Give the extent of all Plasmodium vivax-infected red blood cells.
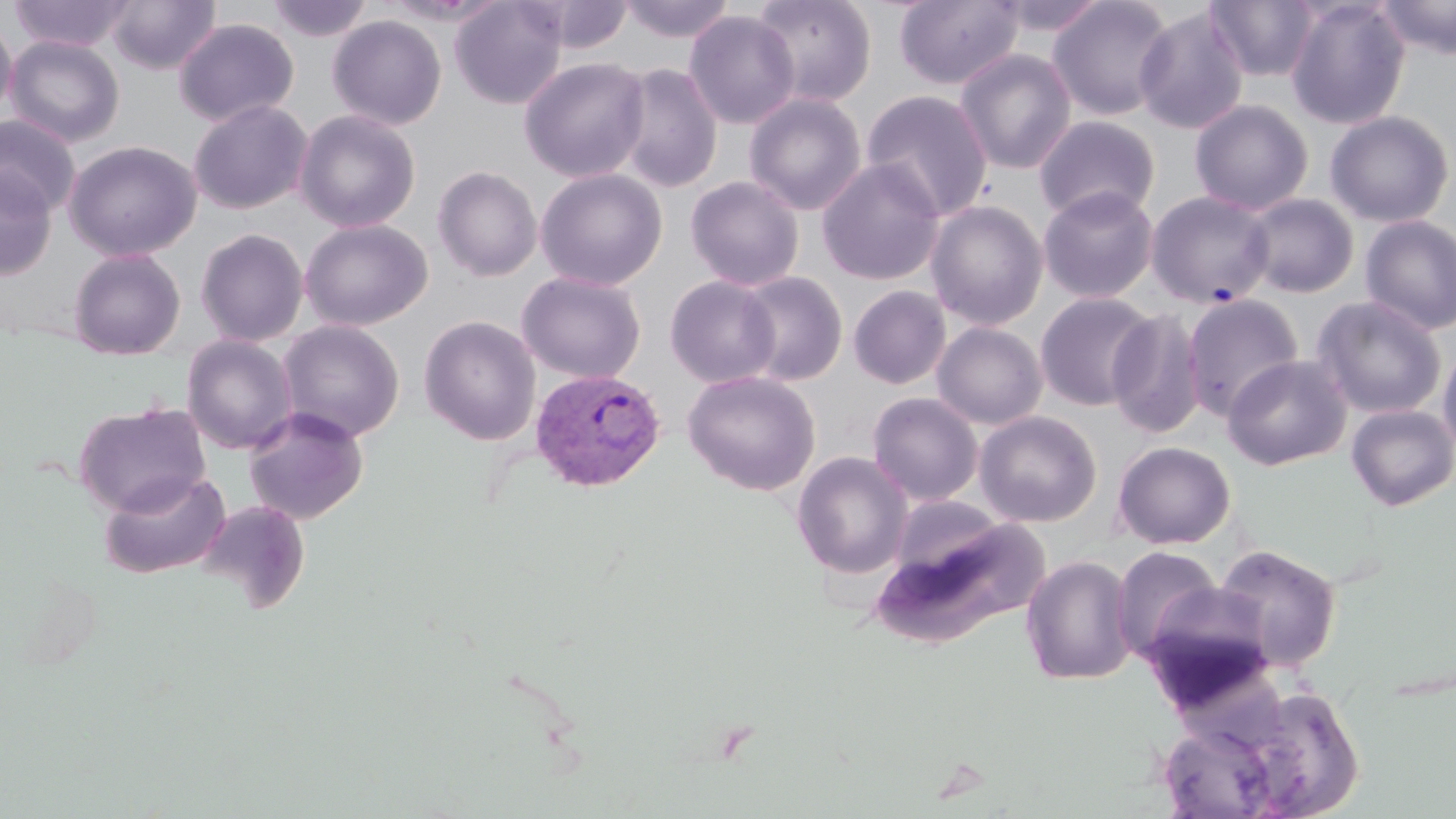

Approximate bounding boxes as named x1/y1/x2/y2 corners in pixels.
Plasmodium vivax-infected red blood cells: (x1=529, y1=368, x2=666, y2=493).

slide-level diagnosis = Plasmodium vivax
modality = light microscopy
preparation = thin blood smear
uninfected red blood cell locations = approximate bounding boxes as named x1/y1/x2/y2 corners in pixels: (x1=8, y1=0, x2=134, y2=52), (x1=106, y1=0, x2=221, y2=74), (x1=267, y1=0, x2=372, y2=43), (x1=450, y1=0, x2=568, y2=109), (x1=528, y1=0, x2=635, y2=53), (x1=621, y1=0, x2=734, y2=43), (x1=751, y1=0, x2=876, y2=107), (x1=893, y1=0, x2=1024, y2=90), (x1=991, y1=0, x2=1109, y2=37), (x1=1047, y1=0, x2=1176, y2=120), (x1=1206, y1=0, x2=1321, y2=82), (x1=1284, y1=0, x2=1412, y2=129), (x1=1375, y1=0, x2=1456, y2=60), (x1=1133, y1=7, x2=1249, y2=135), (x1=684, y1=10, x2=800, y2=129), (x1=0, y1=15, x2=17, y2=123), (x1=328, y1=15, x2=446, y2=130), (x1=173, y1=18, x2=298, y2=127), (x1=4, y1=35, x2=125, y2=147), (x1=954, y1=48, x2=1077, y2=174), (x1=519, y1=56, x2=650, y2=183), (x1=614, y1=64, x2=723, y2=193), (x1=860, y1=89, x2=993, y2=220), (x1=744, y1=93, x2=867, y2=215), (x1=189, y1=99, x2=312, y2=214), (x1=1189, y1=99, x2=1315, y2=215), (x1=295, y1=110, x2=420, y2=232), (x1=1324, y1=110, x2=1455, y2=228), (x1=0, y1=114, x2=81, y2=218), (x1=1034, y1=115, x2=1160, y2=222), (x1=64, y1=140, x2=201, y2=261), (x1=816, y1=159, x2=945, y2=286), (x1=433, y1=166, x2=543, y2=282), (x1=0, y1=167, x2=57, y2=280), (x1=535, y1=168, x2=668, y2=291), (x1=685, y1=175, x2=804, y2=291), (x1=1038, y1=185, x2=1159, y2=303), (x1=1151, y1=192, x2=1278, y2=310), (x1=1241, y1=193, x2=1358, y2=298), (x1=925, y1=200, x2=1049, y2=330), (x1=1359, y1=215, x2=1456, y2=335), (x1=299, y1=219, x2=432, y2=331), (x1=196, y1=228, x2=308, y2=347), (x1=68, y1=248, x2=185, y2=360), (x1=517, y1=271, x2=646, y2=384), (x1=736, y1=271, x2=848, y2=386), (x1=665, y1=275, x2=781, y2=388), (x1=849, y1=285, x2=951, y2=389), (x1=1034, y1=291, x2=1158, y2=411), (x1=1182, y1=294, x2=1304, y2=420), (x1=1311, y1=295, x2=1448, y2=419), (x1=1106, y1=309, x2=1207, y2=438), (x1=419, y1=315, x2=541, y2=445), (x1=277, y1=320, x2=404, y2=443), (x1=932, y1=322, x2=1047, y2=429), (x1=182, y1=335, x2=298, y2=455), (x1=1438, y1=339, x2=1456, y2=459), (x1=1222, y1=355, x2=1352, y2=470), (x1=682, y1=370, x2=820, y2=495), (x1=867, y1=392, x2=984, y2=506), (x1=74, y1=401, x2=210, y2=517), (x1=1345, y1=404, x2=1455, y2=511), (x1=243, y1=406, x2=369, y2=524), (x1=975, y1=410, x2=1102, y2=527), (x1=1113, y1=441, x2=1235, y2=548), (x1=792, y1=452, x2=912, y2=578), (x1=99, y1=470, x2=230, y2=579), (x1=196, y1=499, x2=311, y2=614), (x1=872, y1=504, x2=1046, y2=651), (x1=1213, y1=544, x2=1342, y2=672), (x1=1110, y1=545, x2=1225, y2=664), (x1=1021, y1=554, x2=1137, y2=686), (x1=1222, y1=684, x2=1364, y2=819), (x1=1156, y1=720, x2=1285, y2=818)
magnification = 1000x
stain = May-Grünwald-Giemsa
image size = 1456×819 pixels
field of view = one of a larger specimen